Locate platelets.
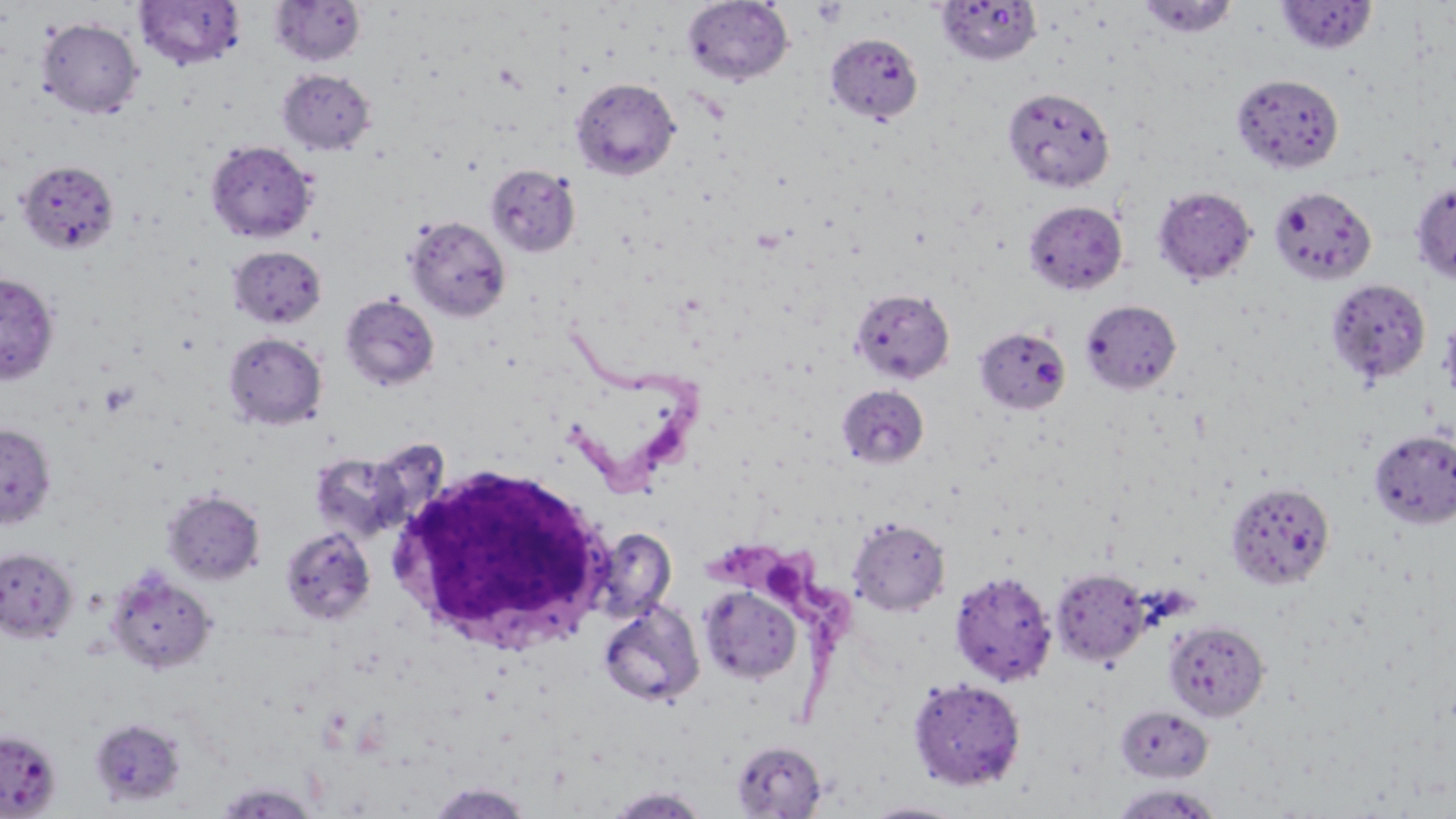
Approximate bounding boxes as [x1, y1, x2, y2] in pixels.
Platelets: [812, 2, 848, 27], [100, 379, 139, 418].

slide-level diagnosis = Trypanosoma brucei
modality = optical microscopy
magnification = 1000x
field of view = single
Trypanosoma brucei locations = approximate bounding boxes as [x1, y1, x2, y2] in pixels: [558, 326, 708, 498], [700, 541, 841, 713]
white blood cell locations = approximate bounding boxes as [x1, y1, x2, y2] in pixels: [388, 460, 613, 658]
uninfected red blood cell locations = approximate bounding boxes as [x1, y1, x2, y2] in pixels: [682, 0, 794, 86], [1138, 0, 1239, 39], [134, 1, 246, 70], [269, 1, 366, 66], [936, 1, 1043, 66], [1275, 1, 1378, 54], [36, 17, 143, 118], [825, 33, 923, 123], [277, 69, 376, 156], [1230, 73, 1345, 174], [570, 77, 681, 180], [1003, 87, 1115, 193], [205, 140, 318, 243], [17, 159, 119, 255], [485, 164, 581, 257], [1410, 182, 1456, 285], [1153, 185, 1257, 285], [1268, 185, 1377, 286], [1024, 200, 1128, 295], [404, 216, 511, 323], [228, 245, 327, 329], [0, 272, 59, 385], [1326, 278, 1431, 387], [850, 287, 955, 384], [339, 293, 440, 391], [1081, 299, 1182, 395], [1439, 314, 1456, 409], [974, 326, 1071, 415], [223, 332, 327, 430], [836, 385, 929, 469], [0, 423, 56, 528], [1369, 429, 1456, 529], [310, 451, 410, 542], [1225, 481, 1336, 591], [162, 489, 265, 585], [848, 517, 950, 616], [589, 526, 677, 625], [280, 527, 376, 626], [0, 547, 78, 643], [105, 566, 218, 675], [1050, 568, 1150, 666], [950, 570, 1057, 687], [698, 586, 802, 685], [597, 600, 705, 707], [1163, 620, 1270, 721], [907, 677, 1026, 791], [1116, 705, 1213, 782], [0, 729, 63, 818], [731, 740, 827, 817], [213, 781, 320, 818], [426, 783, 535, 819], [1110, 784, 1222, 819], [606, 787, 710, 818], [862, 800, 972, 818]
stain = May-Grünwald-Giemsa
preparation = thin blood smear
image size = 1456×819 pixels